Comment on the morphology of the red blood cells.
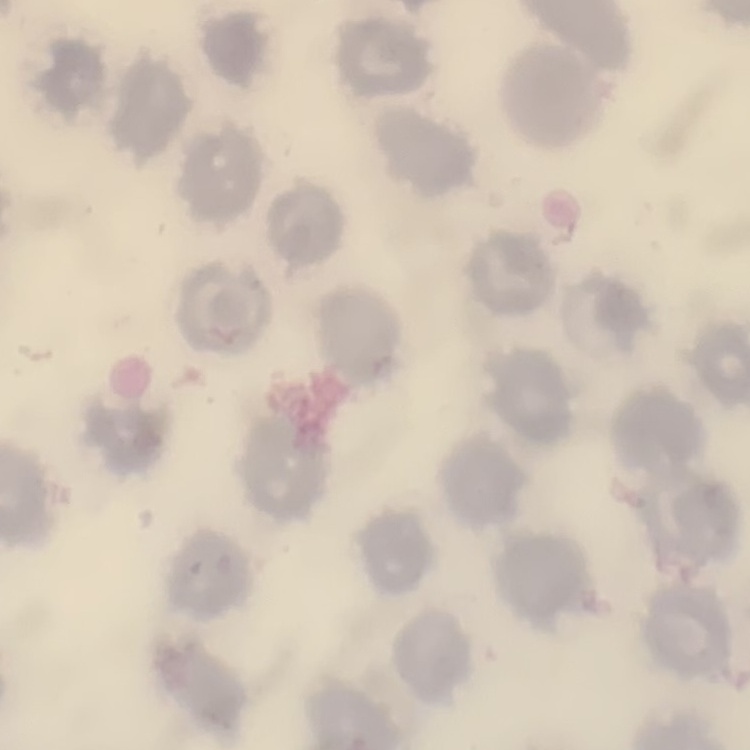

They show no rouleaux formation.

Thin blood film. Square crop of a larger photomicrograph. Stained with either Field's or Giemsa.